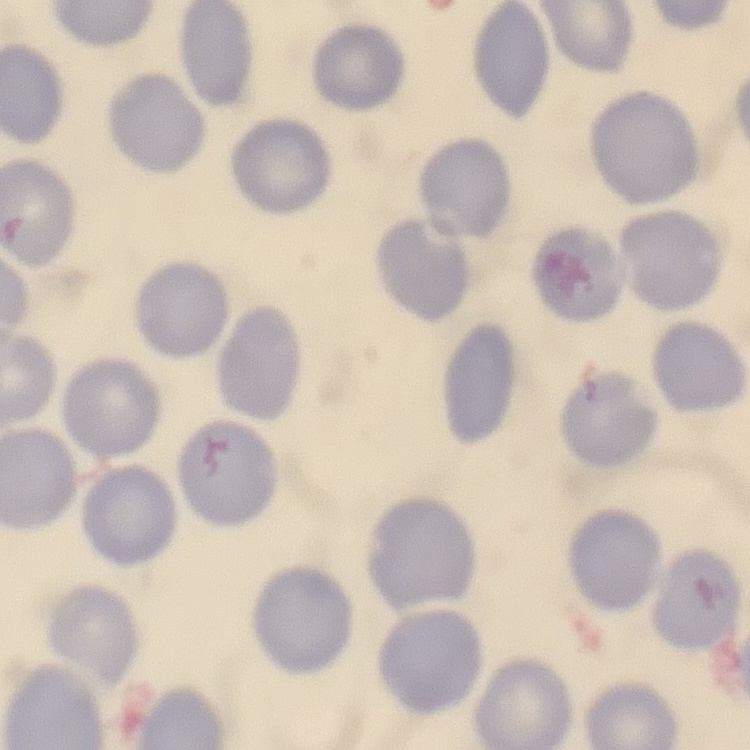
Summary:
  - Erythrocyte morphology: no rouleaux formation
  - Stain: Field's or Giemsa
  - Preparation: thin peripheral smear
  - Image type: square crop of a larger photomicrograph